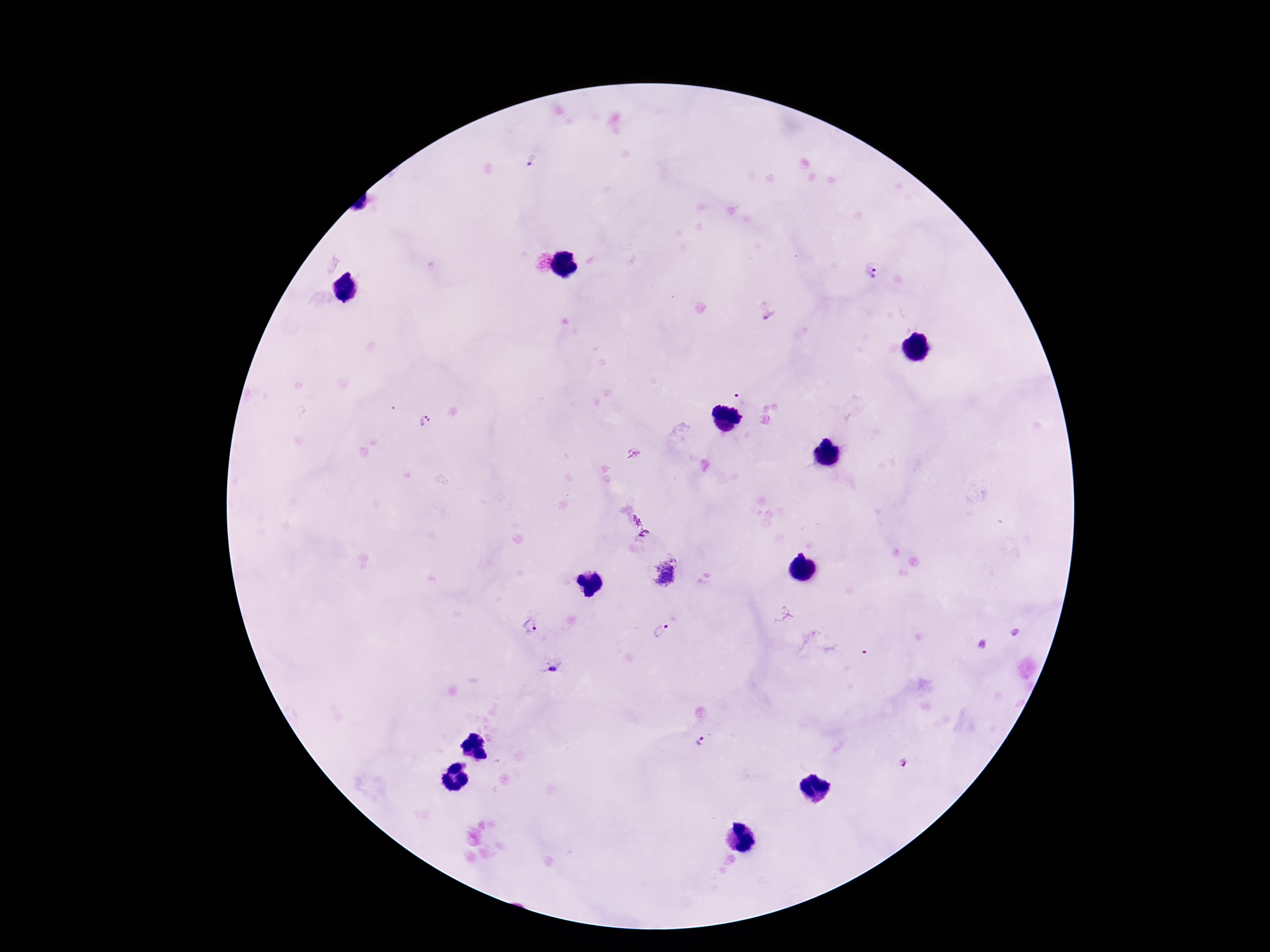
Approximate centers as {x, y} in pixels.
Summary:
  - Plasmodium parasite locations: {532, 162}, {872, 272}, {767, 311}, {742, 398}, {426, 422}, {640, 525}, {665, 573}, {529, 626}, {661, 631}, {553, 670}, {701, 741}, {904, 762}
  - Magnification: 100x
  - Field of view: single
  - Stain: Giemsa
  - Capture: smartphone camera through the microscope eyepiece
  - Patient malaria status: positive
  - Preparation: thick blood film
  - Image size: 1270×952 pixels